Point out each Plasmodium parasite.
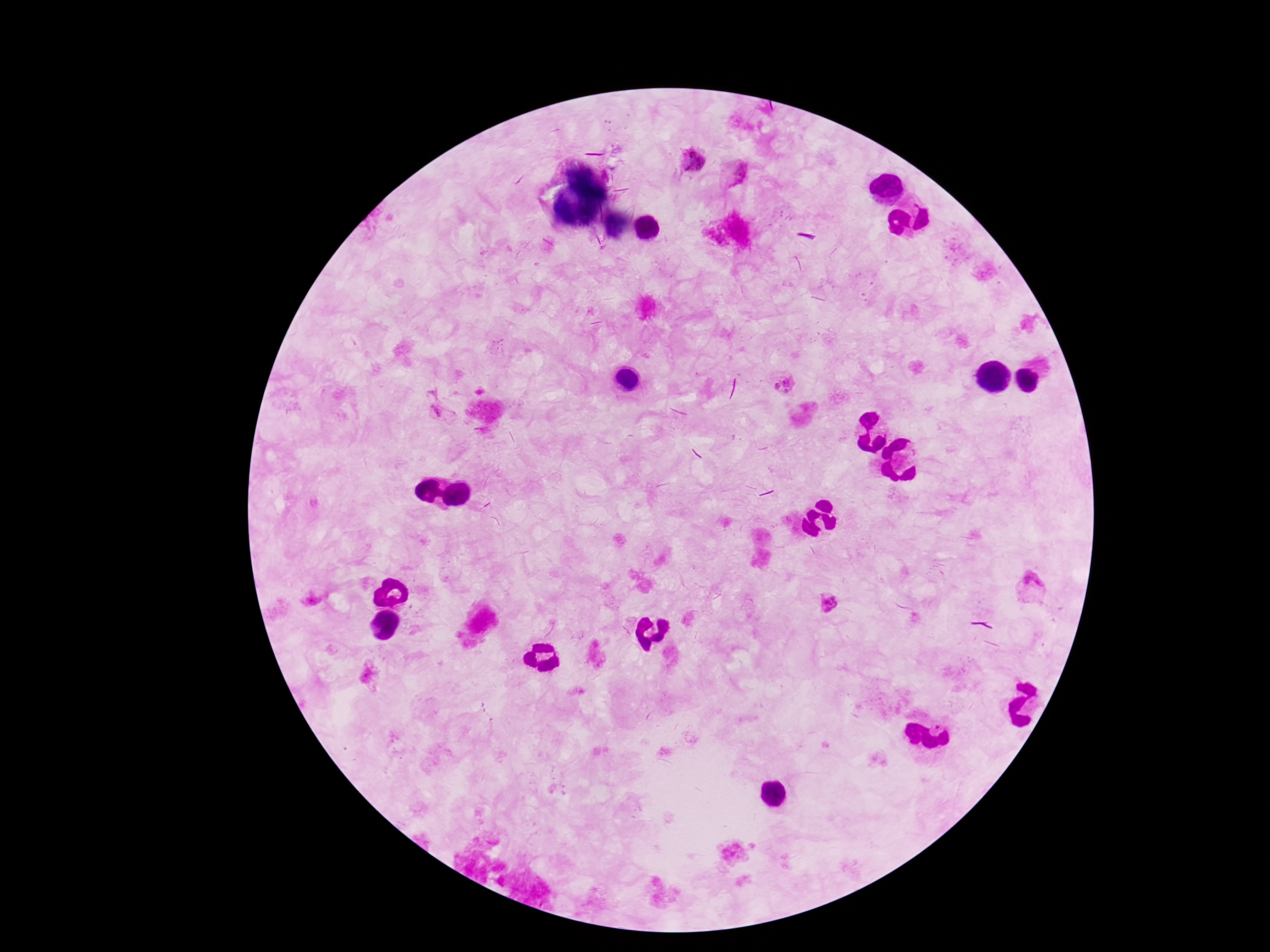
Approximate centers as [x, y] in pixels.
Plasmodium parasites: [689, 159], [736, 174], [782, 379], [439, 415], [1029, 586], [831, 604].

Thick peripheral-blood smear. Image is 1270×952 pixels. Patient malaria status: infected. 100x magnification. Photographed through the microscope eyepiece with a smartphone camera. Giemsa stain. Single field of view.